Identify the blood parasite species.
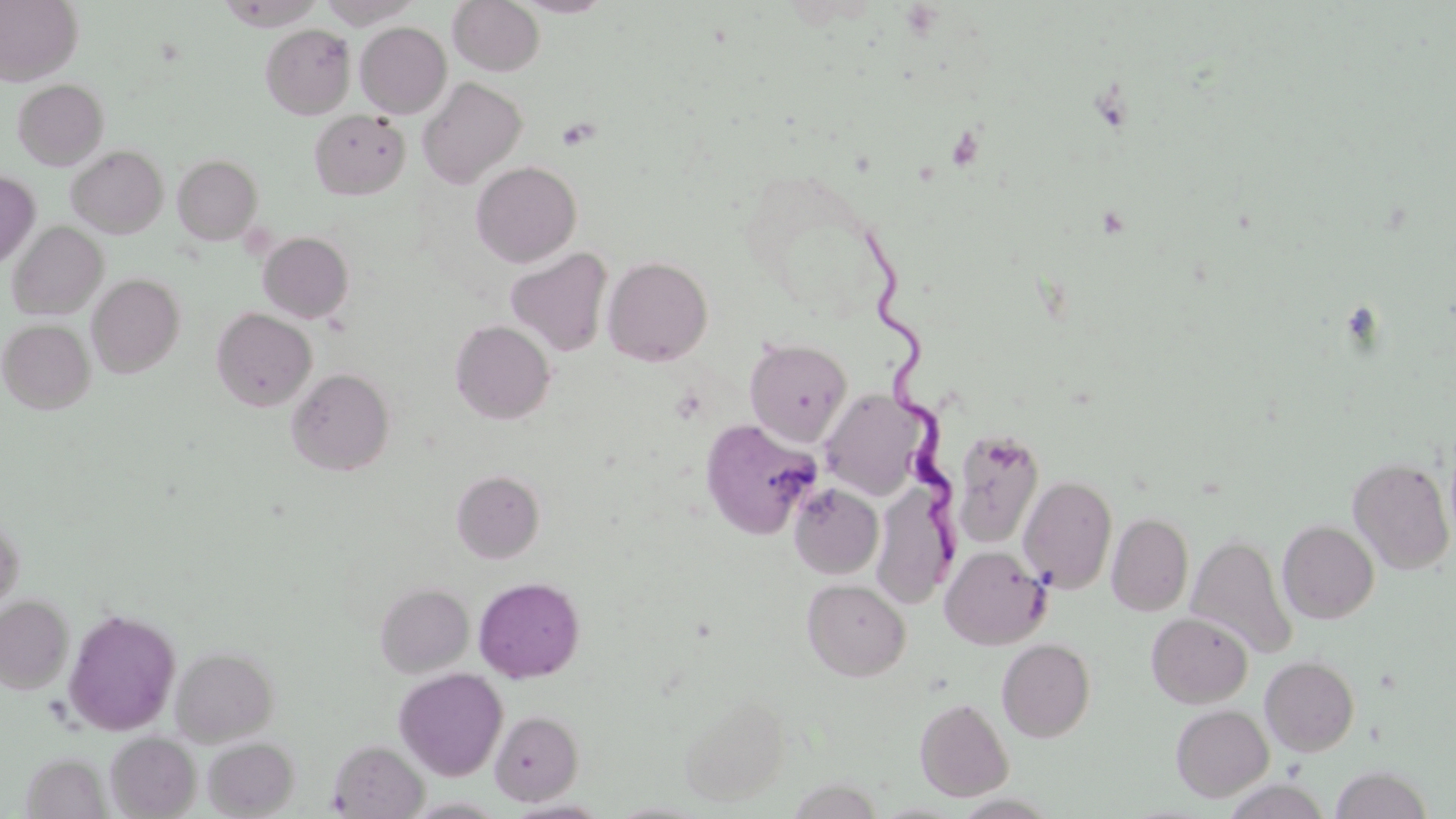

Trypanosoma brucei.

Summary:
  - Coordinate format: approximate bounding boxes as [x1, y1, x2, y2] in pixels
  - Platelet locations: [556, 117, 599, 150]
  - Trypanosoma brucei locations: [858, 226, 965, 560]
  - Uninfected red blood cell locations: [0, 0, 82, 85], [216, 0, 325, 30], [317, 0, 424, 27], [448, 0, 545, 76], [513, 0, 613, 17], [5, 2, 90, 170], [355, 22, 452, 118], [260, 24, 355, 119], [417, 76, 527, 188], [13, 78, 109, 170], [309, 109, 410, 200], [67, 145, 168, 238], [173, 154, 262, 244], [470, 161, 582, 267], [0, 171, 40, 270], [8, 222, 107, 320], [258, 232, 354, 323], [505, 247, 613, 358], [603, 256, 713, 366], [87, 273, 185, 377], [211, 307, 317, 412], [0, 319, 95, 414], [450, 320, 556, 424], [745, 337, 852, 446], [287, 368, 394, 475], [819, 389, 933, 500], [699, 419, 820, 540], [951, 429, 1044, 548], [1348, 456, 1455, 574], [451, 470, 545, 563], [1018, 474, 1117, 594], [788, 482, 883, 579], [872, 482, 957, 608], [1108, 512, 1193, 616], [0, 514, 25, 613], [1278, 520, 1379, 624], [1187, 533, 1297, 660], [940, 544, 1051, 649], [473, 576, 585, 682], [802, 579, 910, 681], [375, 582, 474, 677], [0, 595, 73, 694], [63, 608, 181, 736], [1146, 612, 1253, 708], [997, 638, 1096, 742], [172, 646, 278, 745], [1260, 655, 1359, 756], [394, 667, 508, 780], [679, 692, 790, 806], [915, 697, 1014, 801], [1170, 703, 1273, 802], [490, 710, 584, 805], [106, 732, 201, 818], [203, 737, 299, 817], [328, 739, 428, 818], [20, 753, 111, 818], [1330, 766, 1433, 818], [403, 797, 511, 818], [504, 799, 611, 819]
  - Image size: 1456×819 pixels
  - Preparation: thin blood smear
  - Magnification: 1000x
  - Modality: optical microscopy
  - Stain: May-Grünwald-Giemsa
  - Field of view: one of a larger specimen